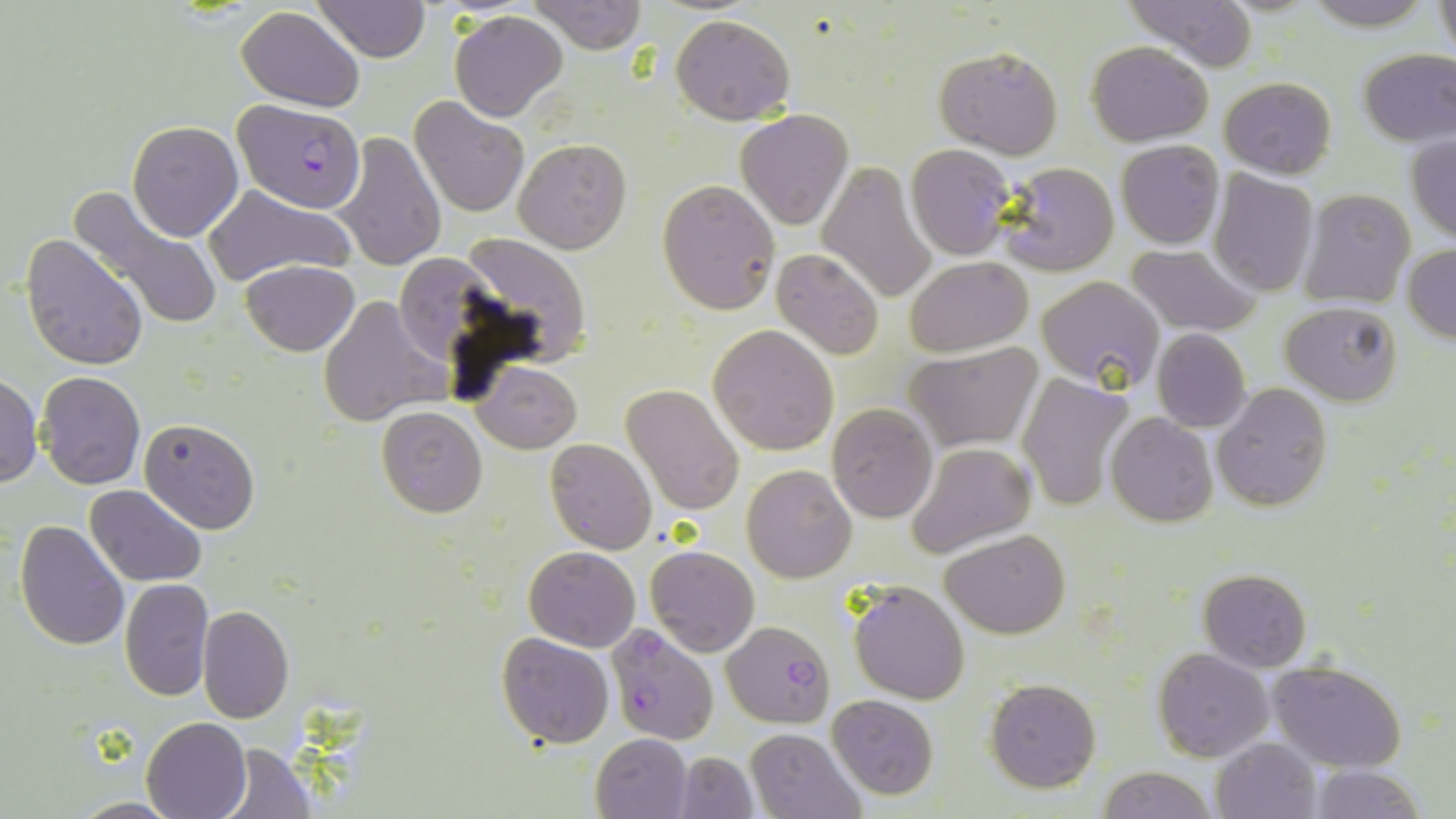

Summary:
  - Coordinate format: approximate bounding boxes as (x1, y1, x2, y2) in pixels
  - Uninfected red blood cell locations: (312, 0, 431, 63), (531, 0, 647, 54), (1126, 0, 1259, 68), (1297, 0, 1442, 29), (1434, 1, 1455, 61), (235, 7, 365, 110), (450, 11, 568, 122), (670, 13, 796, 125), (1086, 41, 1212, 146), (935, 45, 1063, 159), (1356, 47, 1456, 146), (1220, 76, 1336, 180), (411, 95, 529, 218), (735, 110, 853, 228), (350, 111, 512, 251), (129, 120, 243, 241), (335, 133, 446, 271), (1405, 135, 1456, 242), (514, 139, 631, 254), (1116, 139, 1224, 249), (906, 146, 1014, 260), (995, 161, 1118, 277), (816, 162, 938, 304), (1209, 170, 1319, 296), (658, 178, 781, 315), (71, 185, 228, 335), (205, 187, 352, 284), (1299, 189, 1416, 309), (21, 233, 149, 370), (459, 235, 592, 363), (1403, 244, 1456, 343), (1126, 245, 1260, 336), (771, 249, 885, 360), (905, 256, 1032, 355), (240, 260, 359, 355), (1037, 276, 1166, 394), (317, 295, 447, 426), (1280, 301, 1403, 404), (708, 324, 839, 454), (1152, 328, 1251, 431), (903, 342, 1042, 455), (474, 361, 581, 454), (35, 370, 147, 490), (1016, 373, 1133, 512), (0, 375, 43, 488), (621, 383, 745, 518), (1213, 384, 1334, 511), (826, 403, 938, 521), (375, 405, 488, 517), (1106, 413, 1218, 528), (140, 419, 260, 533), (544, 439, 659, 555), (908, 441, 1037, 557), (741, 464, 856, 583), (85, 484, 207, 586), (15, 519, 129, 652), (941, 529, 1069, 639), (643, 543, 760, 657), (523, 546, 641, 651), (1199, 569, 1312, 672), (120, 579, 214, 701), (848, 581, 970, 705), (197, 605, 294, 724), (497, 631, 614, 748), (1153, 648, 1272, 762), (1269, 659, 1408, 770), (985, 678, 1100, 792), (827, 694, 939, 801), (141, 716, 251, 819), (745, 728, 866, 819), (590, 733, 692, 819), (1211, 738, 1321, 818), (217, 742, 316, 817), (675, 752, 757, 818), (1304, 764, 1428, 819), (1098, 766, 1215, 819), (70, 796, 180, 817)
  - Plasmodium falciparum-infected red blood cell locations: (234, 100, 367, 213), (722, 620, 836, 727), (605, 624, 718, 746)
  - Slide-level diagnosis: Plasmodium falciparum
  - Field of view: single
  - Preparation: thin blood film
  - Image size: 1456×819 pixels
  - Modality: optical microscopy
  - Stain: May-Grünwald-Giemsa
  - Magnification: 1000x